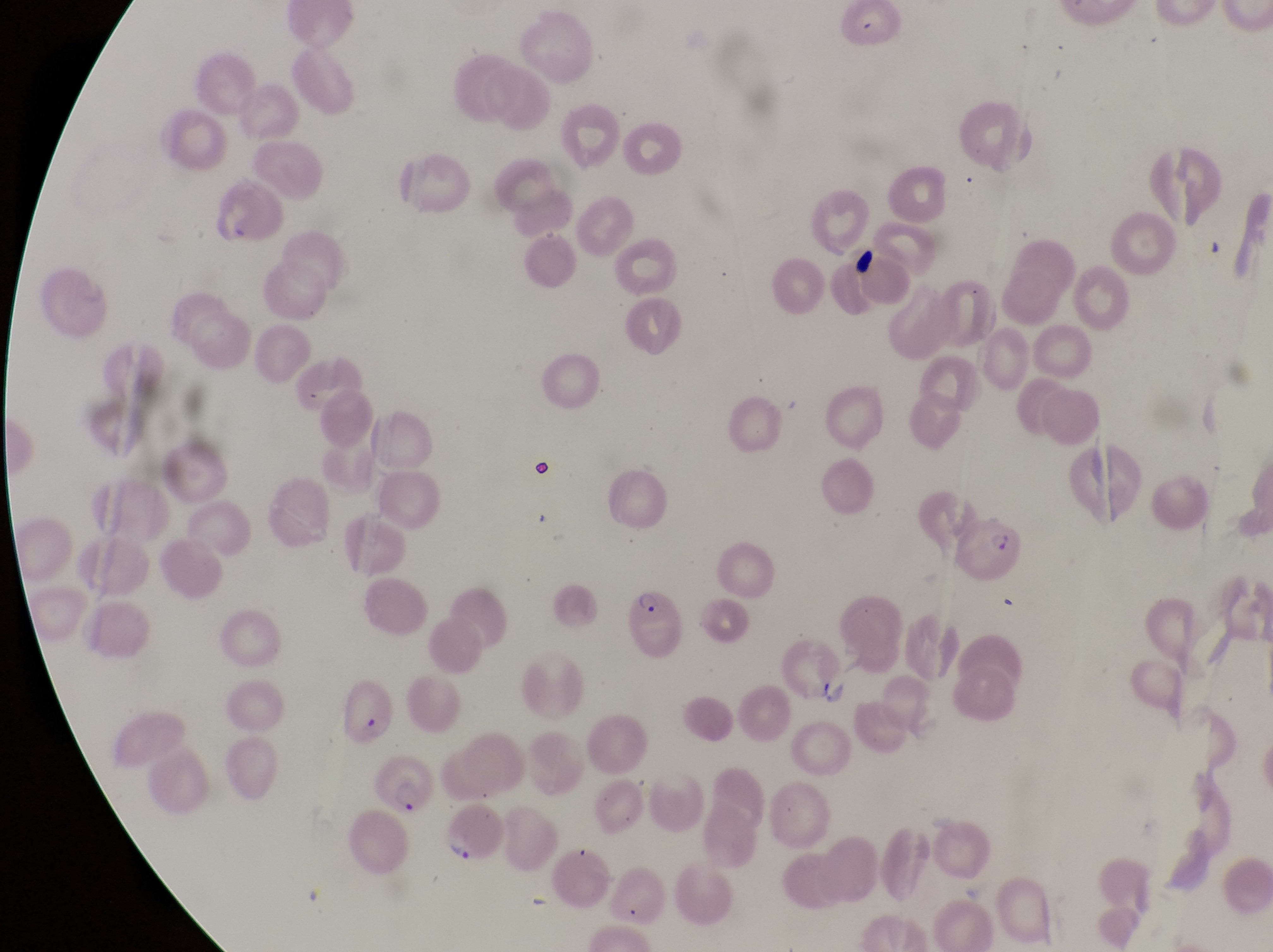
{
  "image_size": "1273×952 pixels",
  "parasitised_red_blood_cell_locations": "approximate bounding boxes as (left, top, right, bottom) in pixels: (961, 512, 1023, 580), (626, 587, 686, 659), (339, 682, 397, 750), (372, 757, 432, 819), (442, 797, 505, 865)",
  "field_of_view": "single",
  "country": "Uganda",
  "magnification": "1000x",
  "capture": "smartphone photograph through the eyepiece of an Olympus CX-23 microscope",
  "preparation": "thin blood film"
}